Assess the morphology of the erythrocytes.
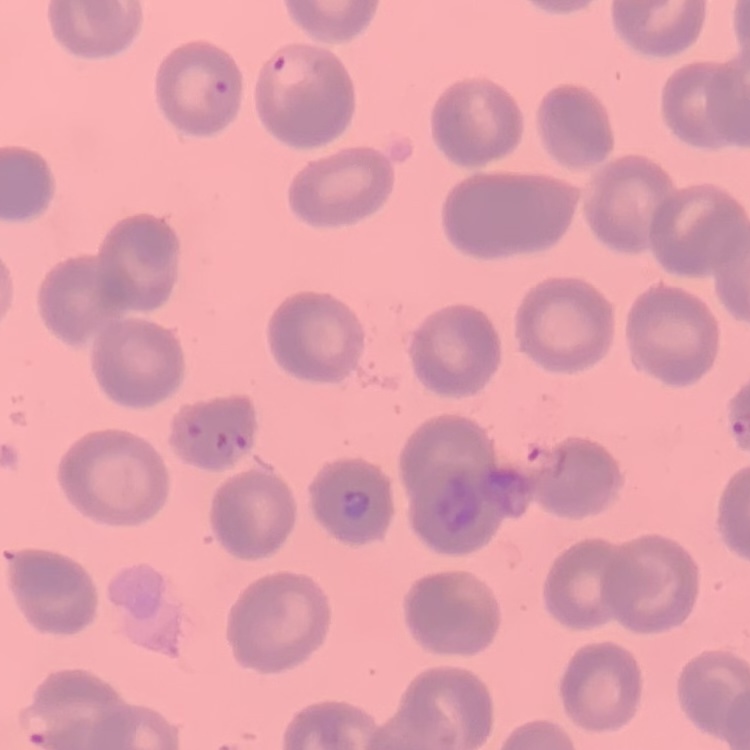

They show no rouleaux formation.

image type = square crop of a larger photomicrograph
preparation = thin blood film
stain = Field's or Giemsa